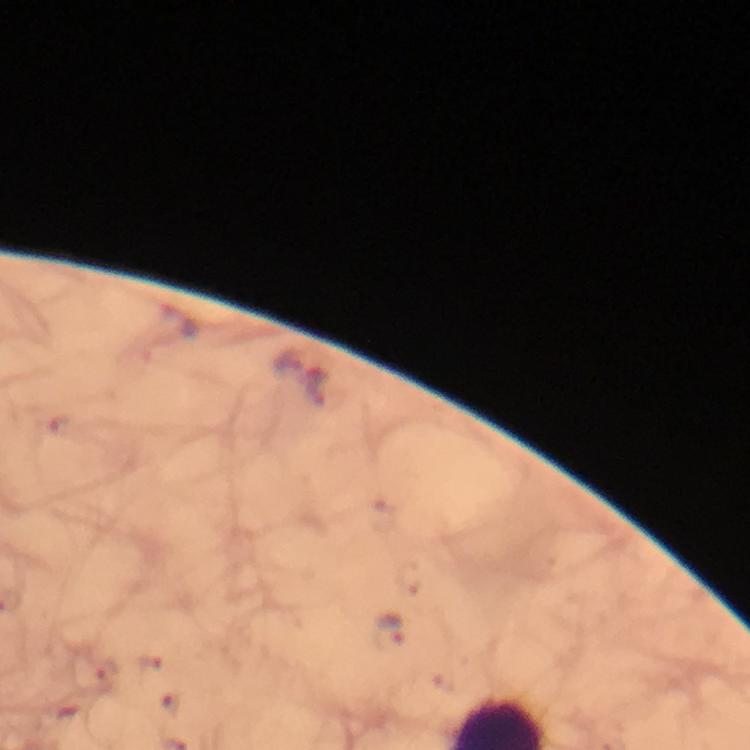

Approximate object centers, in pixels from the top-left corner.
Summary:
  - Malaria parasite locations: (x=316, y=385), (x=389, y=633)
  - Cropped from: one field of view
  - Magnification: 100x
  - Image size: 750×750 pixels
  - Context: from a diagnostic examination for malaria
  - Immersion oil: used
  - Stain: Giemsa
  - Preparation: thick blood smear
  - Capture: smartphone photograph through a microscope